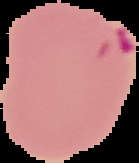

Summary:
  - Result: malaria parasites identified
  - Image type: segmented cell region on a black background
  - Preparation: thin blood smear
  - Image size: 139×163 pixels